Identify the parasite.
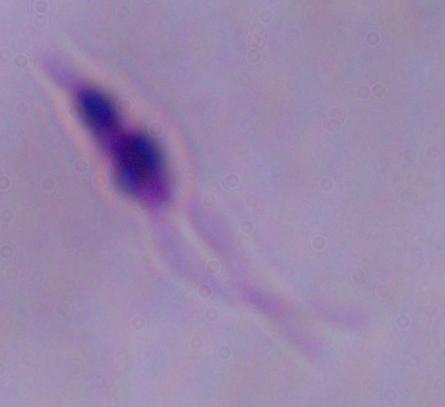

Leishmania.

Summary:
  - Magnification: 1000x
  - Modality: micrograph